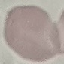
Result: no malaria parasites seen. Giemsa stain. Photographed with a smartphone camera at the microscope eyepiece. Thin smear of blood. Cell patch, automatically extracted from a larger field of view and resized to 64 × 64 pixels.